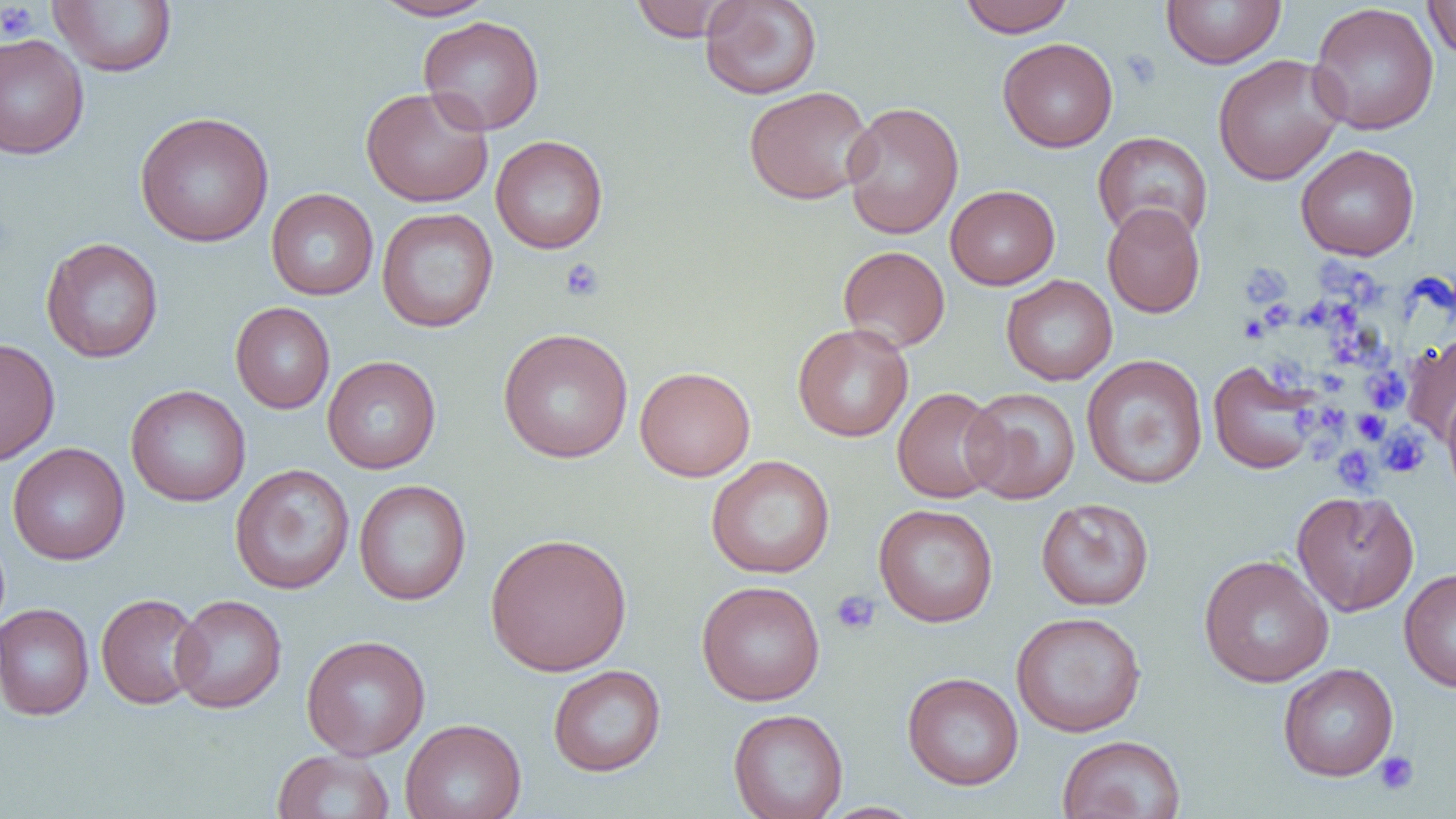
Summary:
  - Coordinate format: approximate bounding boxes as named x1/y1/x2/y2 corners in pixels
  - Uninfected red blood cell locations: (x1=371, y1=0, x2=497, y2=21), (x1=629, y1=0, x2=739, y2=42), (x1=699, y1=0, x2=822, y2=100), (x1=958, y1=0, x2=1075, y2=37), (x1=1160, y1=0, x2=1287, y2=69), (x1=47, y1=1, x2=178, y2=77), (x1=1423, y1=1, x2=1456, y2=62), (x1=1307, y1=3, x2=1439, y2=135), (x1=417, y1=15, x2=545, y2=135), (x1=0, y1=33, x2=90, y2=160), (x1=997, y1=37, x2=1119, y2=153), (x1=1212, y1=54, x2=1345, y2=186), (x1=743, y1=85, x2=875, y2=205), (x1=360, y1=86, x2=494, y2=208), (x1=841, y1=101, x2=964, y2=239), (x1=134, y1=111, x2=275, y2=247), (x1=1092, y1=131, x2=1213, y2=243), (x1=490, y1=135, x2=608, y2=254), (x1=1295, y1=144, x2=1420, y2=261), (x1=945, y1=185, x2=1060, y2=290), (x1=266, y1=188, x2=379, y2=300), (x1=1102, y1=203, x2=1205, y2=318), (x1=377, y1=207, x2=498, y2=332), (x1=40, y1=237, x2=164, y2=364), (x1=838, y1=245, x2=951, y2=352), (x1=1001, y1=274, x2=1118, y2=385), (x1=230, y1=302, x2=335, y2=414), (x1=792, y1=323, x2=914, y2=442), (x1=497, y1=328, x2=634, y2=463), (x1=1401, y1=332, x2=1456, y2=444), (x1=0, y1=338, x2=60, y2=467), (x1=1081, y1=353, x2=1208, y2=490), (x1=322, y1=355, x2=441, y2=474), (x1=1207, y1=359, x2=1322, y2=475), (x1=634, y1=366, x2=755, y2=481), (x1=125, y1=385, x2=251, y2=507), (x1=892, y1=387, x2=1006, y2=504), (x1=962, y1=387, x2=1080, y2=504), (x1=1442, y1=390, x2=1456, y2=501), (x1=7, y1=443, x2=130, y2=565), (x1=706, y1=455, x2=836, y2=579), (x1=230, y1=463, x2=355, y2=595), (x1=354, y1=480, x2=471, y2=606), (x1=1291, y1=490, x2=1420, y2=616), (x1=1036, y1=497, x2=1154, y2=611), (x1=873, y1=503, x2=999, y2=628), (x1=484, y1=532, x2=633, y2=676), (x1=1198, y1=554, x2=1334, y2=688), (x1=1399, y1=568, x2=1456, y2=692), (x1=696, y1=580, x2=826, y2=706), (x1=95, y1=593, x2=206, y2=710), (x1=170, y1=594, x2=287, y2=714), (x1=0, y1=603, x2=95, y2=721), (x1=1010, y1=611, x2=1147, y2=737), (x1=301, y1=634, x2=431, y2=760), (x1=1278, y1=663, x2=1399, y2=781), (x1=548, y1=664, x2=666, y2=777), (x1=902, y1=672, x2=1024, y2=790), (x1=728, y1=708, x2=848, y2=819), (x1=400, y1=718, x2=526, y2=819), (x1=1057, y1=734, x2=1186, y2=819), (x1=272, y1=749, x2=396, y2=819), (x1=814, y1=802, x2=927, y2=819)
  - Platelet locations: (x1=0, y1=2, x2=39, y2=42), (x1=1124, y1=50, x2=1161, y2=88), (x1=558, y1=258, x2=605, y2=302), (x1=1322, y1=258, x2=1347, y2=296), (x1=1240, y1=264, x2=1290, y2=307), (x1=1354, y1=273, x2=1380, y2=306), (x1=1303, y1=299, x2=1333, y2=330), (x1=1331, y1=299, x2=1363, y2=336), (x1=1258, y1=302, x2=1293, y2=328), (x1=1240, y1=315, x2=1269, y2=342), (x1=1333, y1=336, x2=1371, y2=361), (x1=1276, y1=362, x2=1306, y2=388), (x1=1363, y1=368, x2=1409, y2=414), (x1=1321, y1=369, x2=1346, y2=392), (x1=1325, y1=403, x2=1347, y2=431), (x1=1294, y1=406, x2=1314, y2=430), (x1=1352, y1=410, x2=1388, y2=444), (x1=1377, y1=426, x2=1429, y2=478), (x1=1331, y1=445, x2=1379, y2=494), (x1=830, y1=589, x2=881, y2=636), (x1=1375, y1=751, x2=1419, y2=795)
  - Slide-level diagnosis: no evidence of blood parasites
  - Image size: 1456×819 pixels
  - Modality: optical microscopy
  - Preparation: thin blood smear
  - Magnification: 1000x
  - Field of view: one of a larger specimen